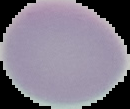

Summary:
  - Image type: cell region segmented out of the field of view; surrounding area masked to black
  - Image size: 130×109 pixels
  - Preparation: thin blood smear
  - Malaria status: uninfected